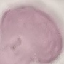

{
  "result": "negative for malaria parasites",
  "preparation": "thin blood smear",
  "image_type": "cell patch, automatically extracted from a larger field of view and resized to 64 × 64 pixels",
  "capture": "smartphone camera at the microscope eyepiece",
  "stain": "Giemsa"
}